Assess the morphology of the red blood cells.
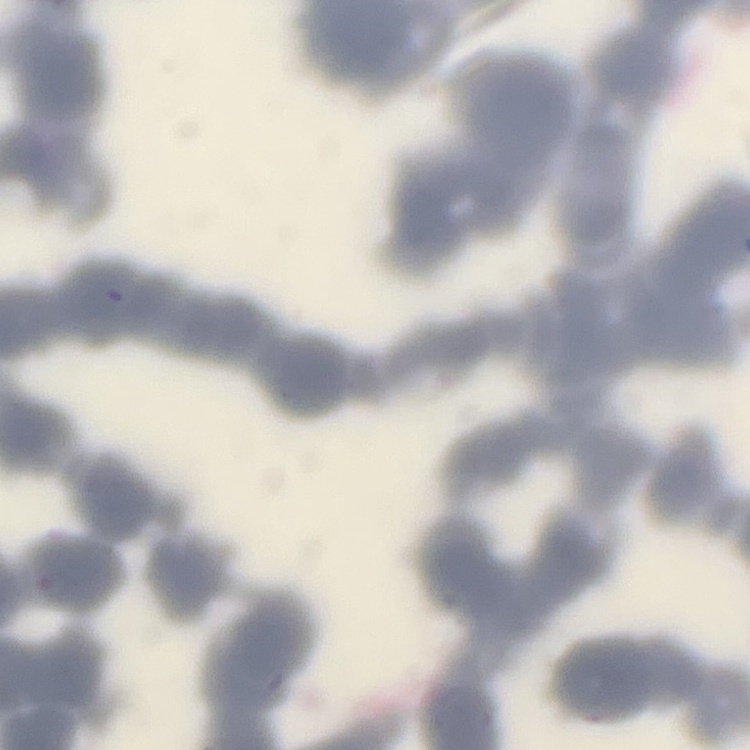

Rouleaux formation.

preparation = thin blood smear
stain = Field's or Giemsa
image type = square crop of a larger photomicrograph